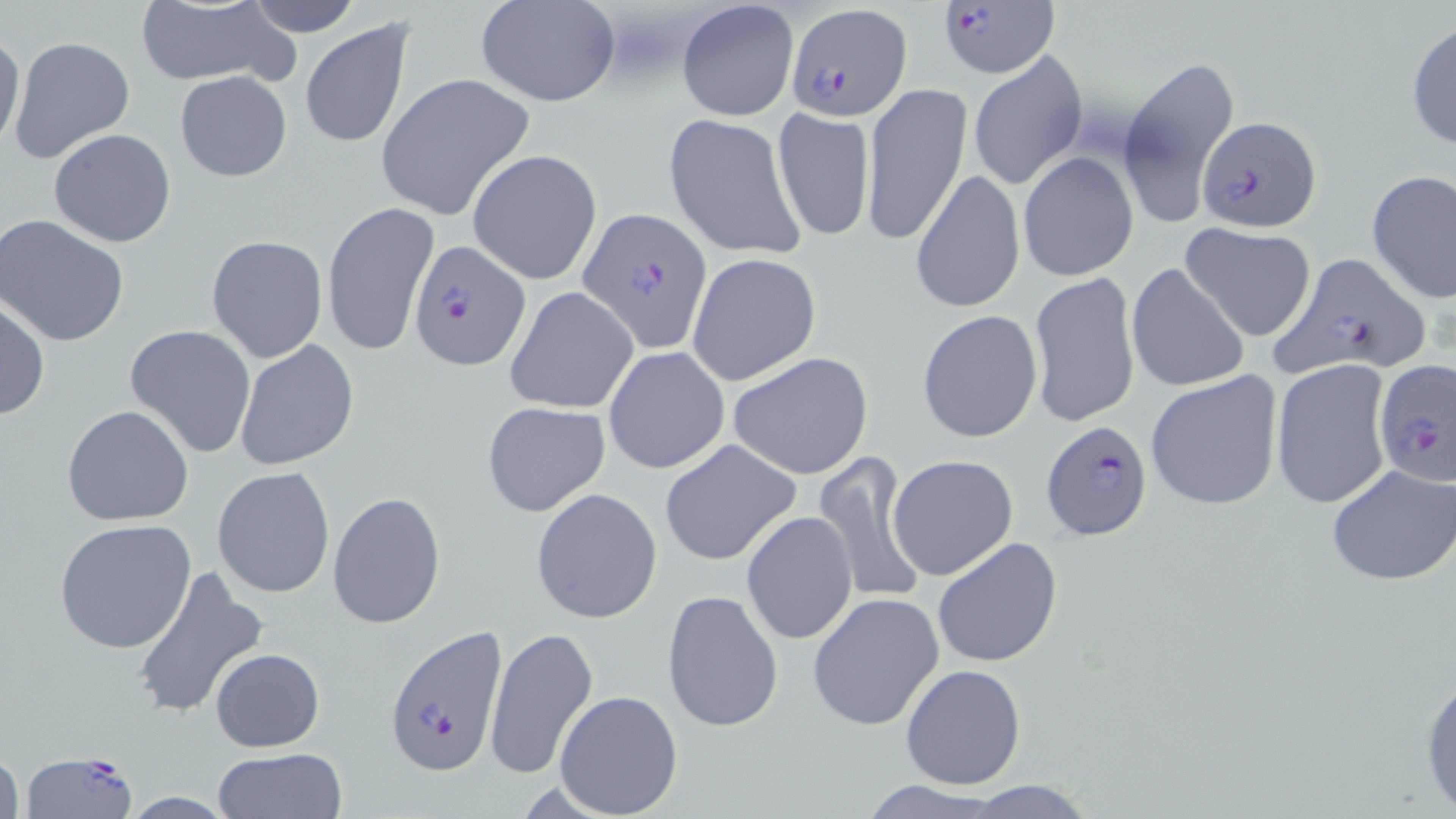
Summary:
  - Coordinate format: approximate bounding boxes as (x1,y1)-(x2,y2) corner pairs in pixels
  - Uninfected red blood cell locations: (242,0)-(363,36), (134,1)-(291,87), (474,1)-(621,108), (676,1)-(799,122), (303,19)-(415,148), (1407,21)-(1456,154), (0,31)-(25,156), (8,35)-(136,166), (967,48)-(1087,192), (1117,56)-(1241,225), (174,69)-(293,182), (376,73)-(537,222), (862,83)-(972,247), (771,107)-(876,243), (662,113)-(808,260), (49,127)-(177,247), (468,149)-(602,284), (1018,151)-(1137,282), (911,170)-(1024,315), (1367,170)-(1456,304), (323,201)-(439,356), (0,213)-(131,345), (1177,223)-(1318,344), (206,236)-(327,363), (686,254)-(822,387), (1125,262)-(1251,394), (1028,271)-(1140,428), (505,286)-(639,415), (0,297)-(49,422), (917,310)-(1043,444), (124,323)-(257,458), (234,338)-(359,469), (602,345)-(730,474), (728,351)-(875,481), (1271,359)-(1395,512), (1144,370)-(1283,511), (481,401)-(611,517), (62,404)-(194,527), (660,439)-(801,566), (811,451)-(930,605), (888,454)-(1019,580), (1326,464)-(1455,586), (213,467)-(335,599), (531,488)-(662,624), (329,491)-(446,628), (741,511)-(857,647), (56,519)-(198,654), (933,535)-(1062,668), (133,563)-(268,721), (661,588)-(784,734), (806,592)-(944,731), (484,626)-(598,780), (211,649)-(325,750), (1418,658)-(1456,819), (900,664)-(1026,790), (553,690)-(684,818), (0,744)-(24,819), (212,747)-(348,819), (958,782)-(1101,816)
  - Platelet locations: (605,13)-(686,86)
  - Plasmodium falciparum-infected red blood cell locations: (939,0)-(1057,79), (787,2)-(913,120), (1196,115)-(1321,233), (579,205)-(713,352), (408,240)-(528,371), (1268,250)-(1433,377), (1374,360)-(1456,486), (1041,417)-(1152,539), (380,627)-(507,776), (26,748)-(137,818)
  - Slide-level diagnosis: Plasmodium falciparum
  - Image size: 1456×819 pixels
  - Stain: May-Grünwald-Giemsa
  - Modality: optical microscopy
  - Preparation: thin blood film
  - Field of view: one of a larger specimen
  - Magnification: 1000x